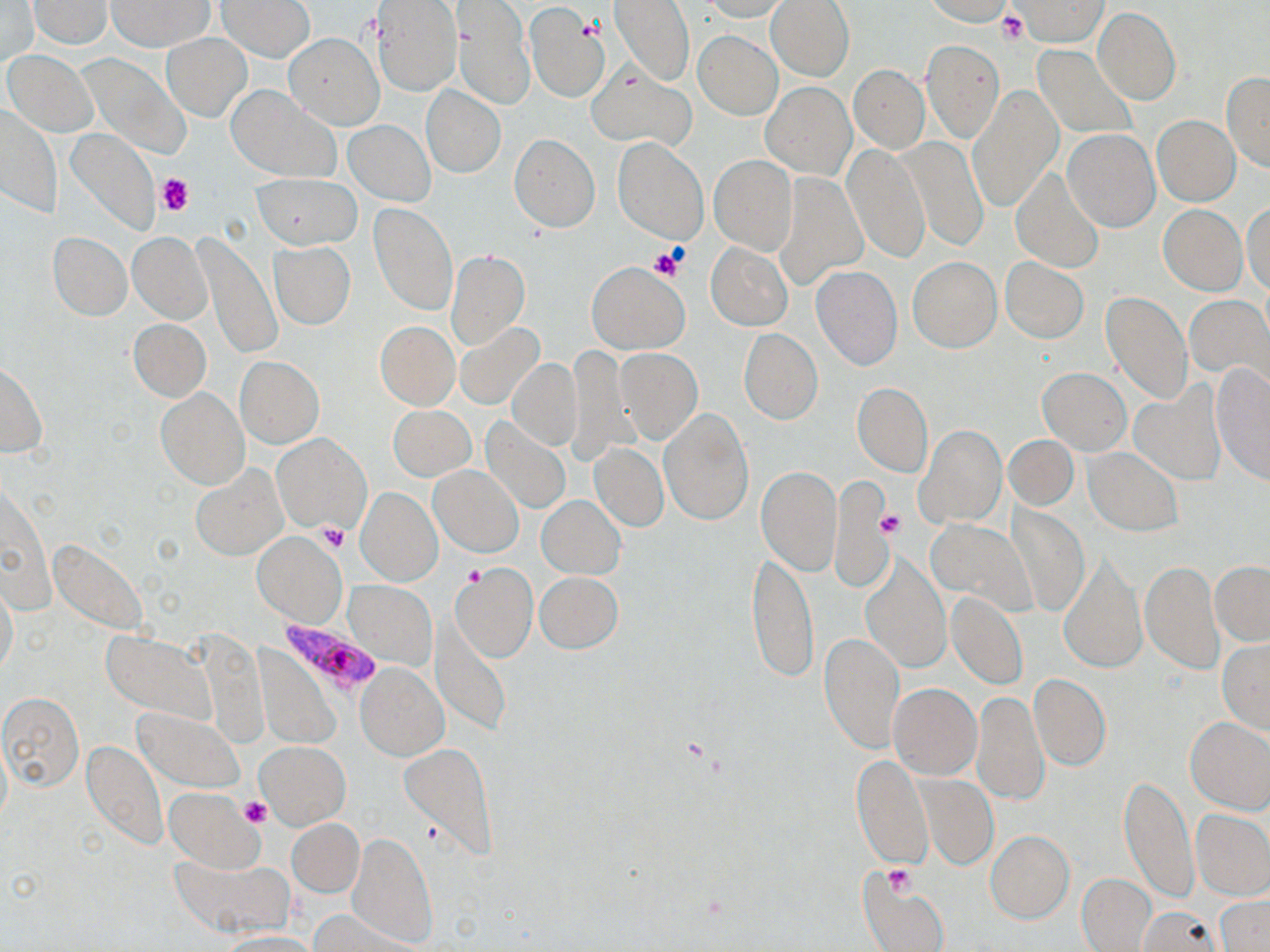

Approximate bounding boxes as (x1,y1)-(x2,y2) corner pairs in pixels. Plasmodium falciparum-infected red blood cell locations: (283,622)-(384,695). Uninfected red blood cell locations: (217,0)-(315,62), (453,0)-(534,110), (609,0)-(695,87), (703,0)-(790,21), (766,0)-(855,82), (1,1)-(39,65), (29,1)-(111,48), (107,1)-(212,50), (370,1)-(461,97), (921,1)-(1013,25), (1012,1)-(1109,47), (523,2)-(610,103), (1093,7)-(1181,105), (694,29)-(782,120), (163,33)-(252,121), (285,33)-(383,129), (921,41)-(1003,143), (1033,46)-(1137,140), (4,52)-(96,135), (587,66)-(697,151), (849,66)-(929,153), (1221,71)-(1270,172), (760,82)-(856,178), (421,84)-(505,177), (225,85)-(341,184), (966,86)-(1062,213), (0,105)-(60,219), (1153,115)-(1240,205), (344,119)-(434,205), (66,128)-(160,235), (1063,129)-(1160,231), (509,134)-(601,232), (612,136)-(709,246), (901,138)-(989,251), (842,143)-(931,264), (708,153)-(797,254), (1011,167)-(1104,272), (773,171)-(868,290), (251,173)-(360,249), (369,201)-(458,317), (1243,201)-(1270,294), (1158,205)-(1247,295), (128,231)-(212,323), (49,232)-(131,320), (194,233)-(283,359), (268,242)-(356,329), (707,242)-(792,330), (446,250)-(529,349), (908,257)-(1001,352), (1001,258)-(1088,343), (587,262)-(688,354), (812,266)-(903,370), (1101,290)-(1192,405), (1185,294)-(1269,387), (129,318)-(211,401), (375,322)-(460,410), (454,323)-(544,409), (739,328)-(823,425), (567,343)-(635,464), (615,348)-(703,444), (235,356)-(323,449), (509,357)-(582,450), (0,359)-(47,458), (1209,362)-(1270,484), (1038,368)-(1130,453), (853,383)-(932,477), (1130,386)-(1225,483), (157,387)-(247,489), (389,405)-(475,480), (659,407)-(753,525), (481,416)-(571,514), (916,426)-(1006,528), (272,435)-(370,533), (1004,435)-(1078,510), (591,442)-(669,532), (1083,447)-(1183,537), (192,465)-(287,560), (430,465)-(523,556), (756,465)-(843,577), (830,476)-(897,590), (356,487)-(443,586), (536,495)-(625,577), (1007,504)-(1090,616), (925,518)-(1037,616), (251,531)-(346,627), (745,548)-(819,683), (1057,553)-(1146,675), (860,554)-(950,674), (1139,560)-(1224,673), (450,562)-(538,663), (1210,563)-(1270,644), (535,572)-(622,653), (345,581)-(435,669), (1,582)-(19,679), (947,592)-(1028,689), (431,620)-(510,739), (100,629)-(220,725), (819,631)-(905,754), (1218,638)-(1270,734), (256,648)-(339,747), (356,662)-(449,760), (1029,673)-(1112,771), (888,683)-(981,779), (971,689)-(1048,808), (0,690)-(84,793), (134,708)-(244,792), (1185,717)-(1270,814), (83,740)-(166,850), (256,740)-(351,830), (400,743)-(496,855), (852,755)-(933,870), (918,776)-(998,869), (1119,776)-(1198,904), (165,787)-(263,870), (1192,810)-(1270,900), (288,818)-(363,897), (986,831)-(1074,923), (346,833)-(436,949), (171,856)-(292,937), (857,871)-(950,952), (1075,873)-(1157,952), (1216,894)-(1269,952), (1135,904)-(1220,952), (310,910)-(418,951), (215,931)-(321,951). Platelet locations: (997,11)-(1026,43), (156,173)-(194,216), (650,248)-(686,279), (877,508)-(906,539), (317,523)-(349,551), (240,798)-(273,829), (883,866)-(917,895). Slide-level diagnosis: Plasmodium falciparum. Image is 1270×952 pixels. May-Grünwald-Giemsa-stained preparation. Thin blood film. Captured at 1000x magnification. One field of a larger specimen. Light microscopy.